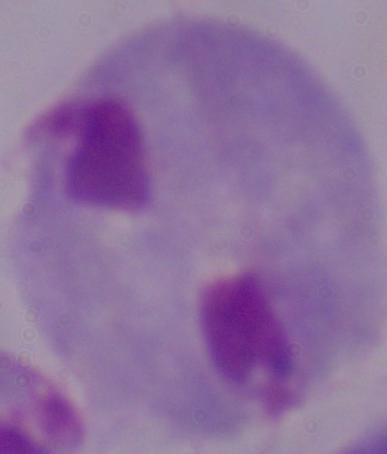 Captured at 1000x magnification. A trichomonad is shown. Photomicrograph.